State which parasite is depicted.
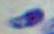

Toxoplasma gondii.

Summary:
  - Magnification: 1000x
  - Modality: photomicrograph